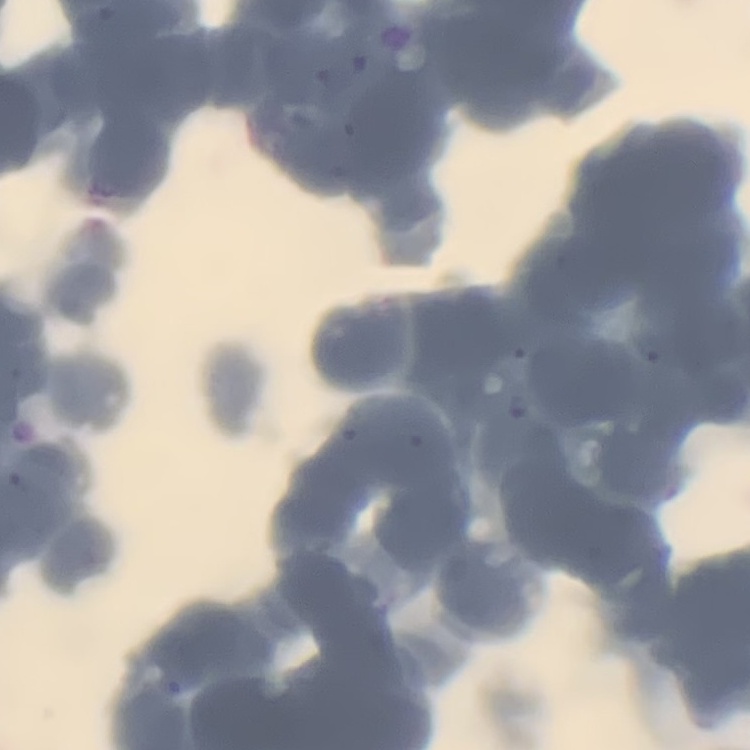

Summary:
  - Erythrocyte morphology: rouleaux formation
  - Image type: one tile cut from a larger photomicrograph
  - Preparation: thin blood film
  - Stain: Field's or Giemsa